Name the parasite shown.
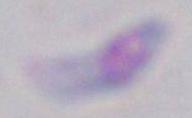

This is Toxoplasma gondii.

1000x magnification. Photomicrograph.